Comment on the morphology of the red blood cells.
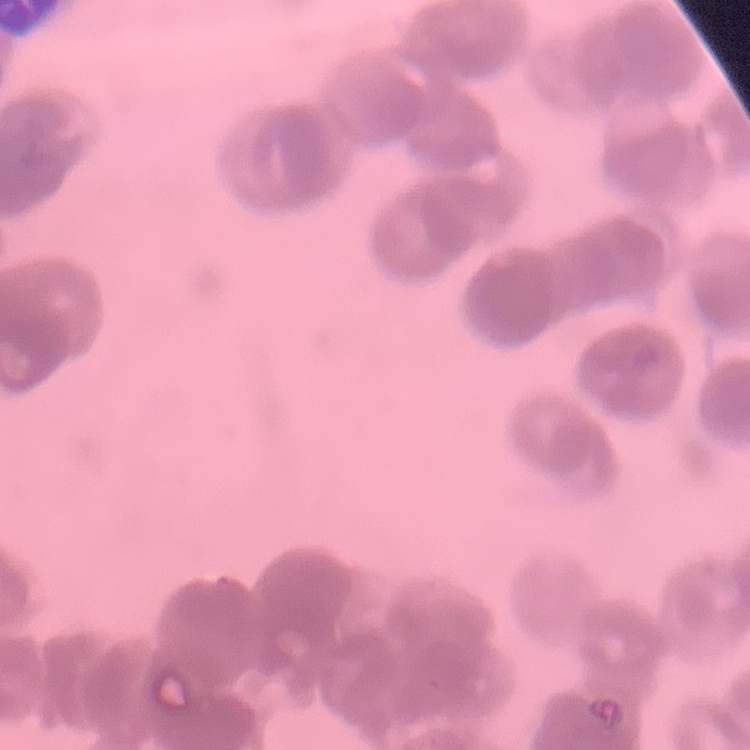
Rouleaux formation.

Summary:
  - Image type: square crop of a larger photomicrograph
  - Preparation: thin blood film
  - Stain: Field's or Giemsa